Comment on the morphology of the erythrocytes.
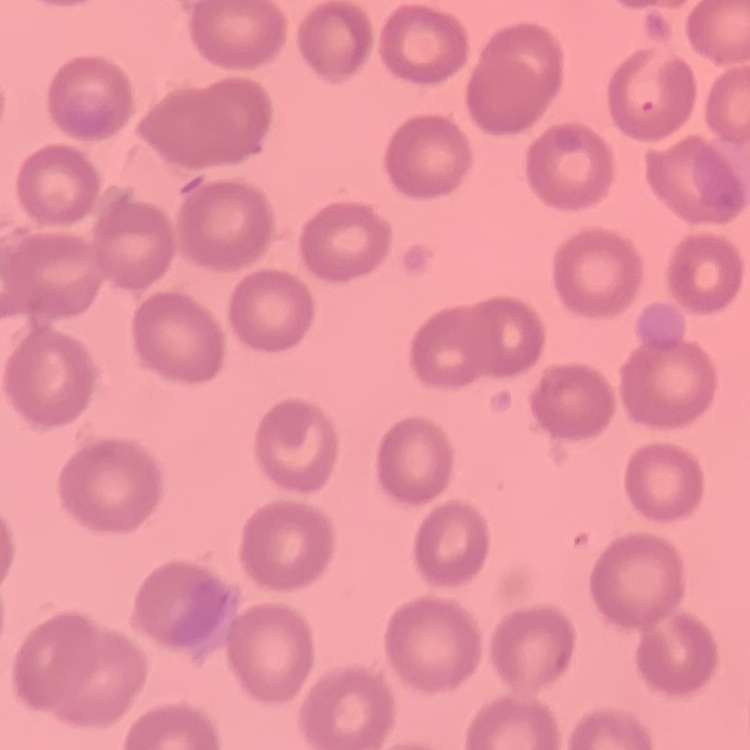

No rouleaux formation.

{
  "image_type": "square crop of a larger photomicrograph",
  "stain": "Field's or Giemsa",
  "preparation": "thin blood smear"
}